Assess the morphology of the erythrocytes.
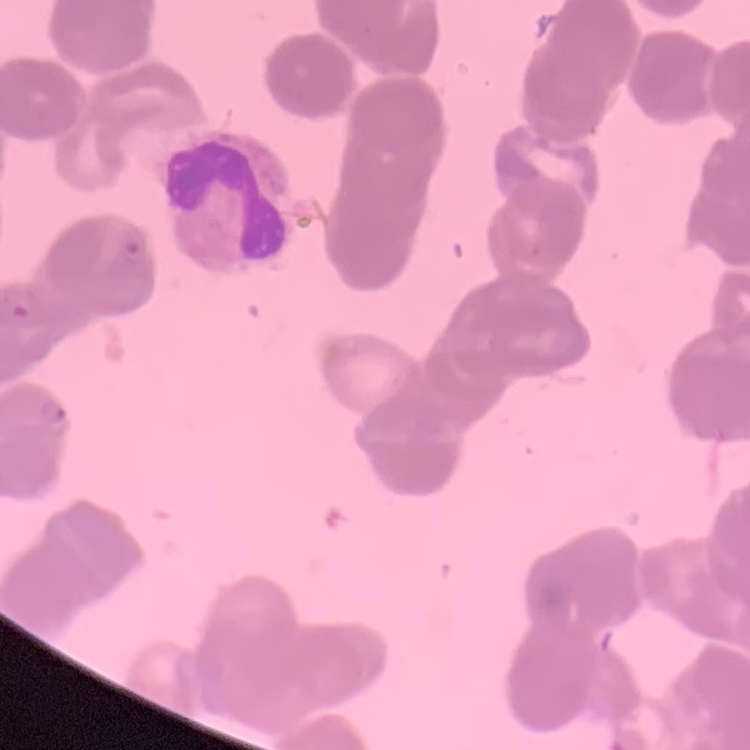
They show rouleaux formation.

Summary:
  - Stain: Field's or Giemsa
  - Image type: square crop of a larger photomicrograph
  - Preparation: thin blood film